Locate and identify every blood parasite.
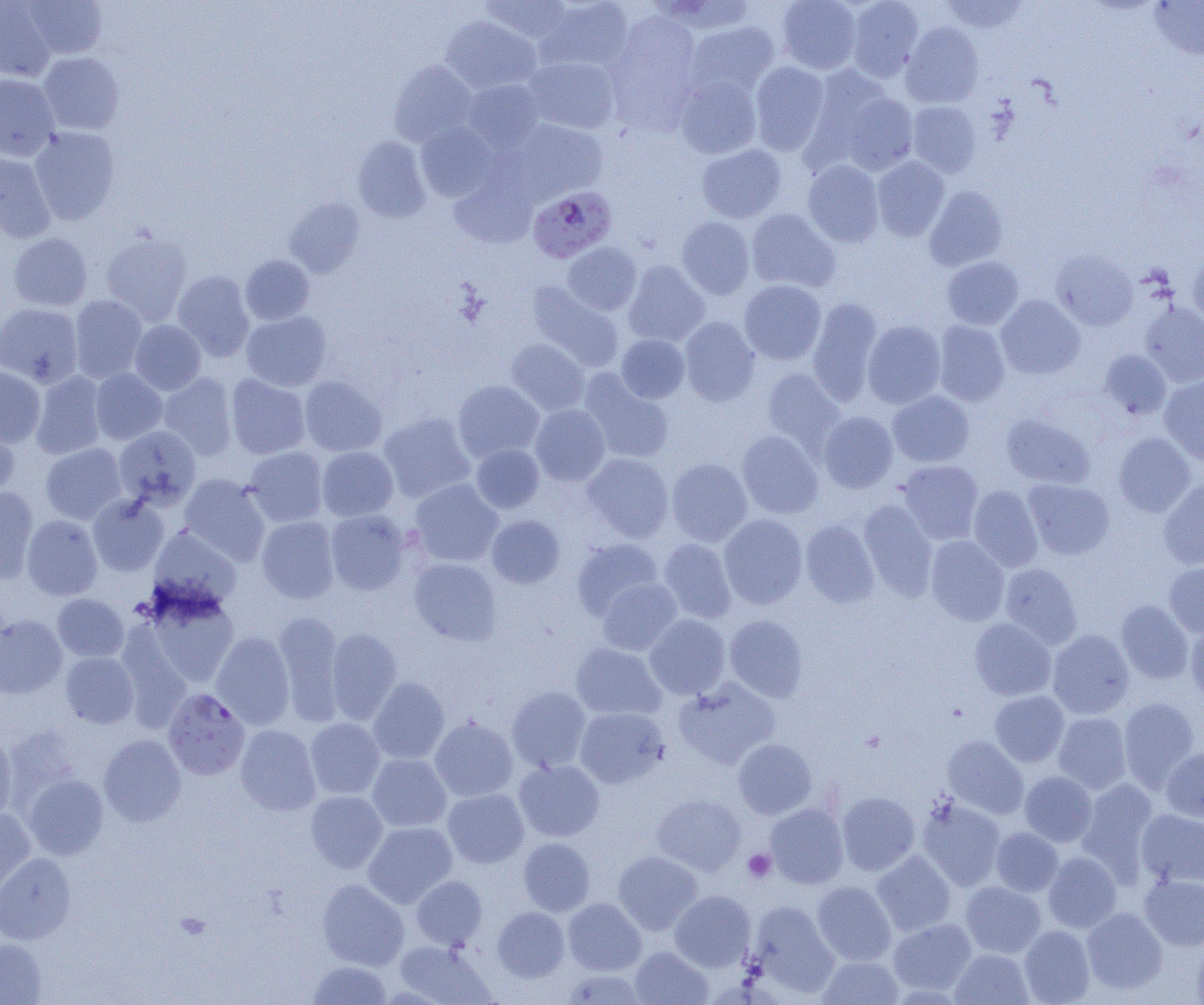

Approximate bounding boxes as (x1,y1)-(x2,y2) corner pairs in pixels.
Plasmodium falciparum-infected red blood cells: (528,186)-(616,262), (163,688)-(250,780).
No Plasmodium ovale, Plasmodium malariae, Plasmodium vivax, Babesia divergens, or Trypanosoma brucei observed.

Uninfected red blood cell locations: (22,0)-(107,59), (480,0)-(572,44), (536,0)-(634,73), (663,0)-(758,34), (776,0)-(862,73), (845,0)-(923,81), (0,1)-(57,81), (939,1)-(1029,35), (1149,1)-(1204,60), (605,13)-(703,126), (441,16)-(541,94), (686,21)-(780,97), (901,22)-(984,108), (38,52)-(124,134), (524,56)-(620,134), (389,60)-(478,146), (750,61)-(830,155), (0,73)-(60,161), (674,74)-(761,159), (461,79)-(545,153), (824,82)-(920,176), (907,101)-(982,177), (511,119)-(608,201), (415,122)-(499,202), (29,127)-(120,225), (352,136)-(431,222), (696,143)-(786,223), (0,149)-(55,243), (872,156)-(950,241), (803,160)-(884,247), (449,172)-(537,249), (924,186)-(1008,271), (284,198)-(365,278), (746,209)-(841,293), (676,216)-(755,300), (7,232)-(93,311), (100,233)-(193,325), (562,242)-(642,315), (1187,249)-(1204,329), (1051,250)-(1138,331), (240,255)-(314,325), (941,256)-(1024,330), (623,260)-(710,347), (172,270)-(254,361), (739,279)-(826,365), (526,281)-(624,372), (69,295)-(147,383), (995,295)-(1085,379), (807,297)-(884,407), (0,302)-(82,387), (1140,302)-(1204,387), (241,311)-(332,391), (679,316)-(760,406), (130,320)-(206,395), (862,320)-(946,409), (932,321)-(1010,406), (616,334)-(690,403), (505,338)-(590,416), (1098,349)-(1171,420), (0,366)-(45,447), (761,367)-(846,456), (90,368)-(167,444), (579,370)-(674,464), (31,371)-(107,459), (158,373)-(237,460), (225,374)-(311,460), (299,375)-(387,457), (1160,376)-(1204,466), (453,380)-(545,462), (887,390)-(974,467), (530,404)-(610,486), (818,411)-(898,493), (378,412)-(476,503), (1001,413)-(1095,488), (0,423)-(19,503), (113,425)-(201,510), (737,430)-(823,519), (1113,433)-(1196,517), (40,443)-(126,523), (471,444)-(544,513), (317,446)-(398,521), (243,447)-(328,527), (582,453)-(674,543), (667,458)-(752,546), (897,460)-(984,544), (179,474)-(270,566), (1158,478)-(1204,569), (409,479)-(503,567), (1023,479)-(1115,560), (968,485)-(1043,572), (0,486)-(39,582), (88,494)-(169,576), (858,500)-(938,600), (325,509)-(412,595), (487,514)-(565,589), (718,514)-(808,609), (21,515)-(102,600), (256,516)-(339,604), (800,519)-(879,608), (148,526)-(242,611), (926,535)-(1010,625), (571,538)-(664,621), (658,538)-(736,623), (409,558)-(502,645), (999,562)-(1082,649), (1164,562)-(1204,637), (596,578)-(682,656), (140,589)-(240,689), (52,593)-(128,661), (1116,600)-(1193,684), (273,612)-(345,726), (0,614)-(67,698), (644,614)-(730,699), (725,615)-(808,702), (969,617)-(1056,701), (1185,621)-(1204,707), (125,625)-(196,738), (326,627)-(402,725), (1047,629)-(1134,719), (211,631)-(295,729), (570,643)-(666,720), (60,652)-(139,728), (368,677)-(450,764), (674,678)-(780,769), (506,686)-(591,772), (989,690)-(1069,767), (1118,696)-(1201,791), (574,707)-(668,788), (1052,712)-(1131,793), (430,717)-(518,802), (305,718)-(385,799), (235,724)-(321,816), (0,733)-(17,823), (98,735)-(186,826), (942,735)-(1028,819), (733,738)-(817,819), (1161,747)-(1204,822), (367,753)-(451,832), (514,759)-(604,841), (1019,771)-(1097,846), (23,774)-(108,860), (1076,778)-(1159,880), (442,788)-(529,868), (306,791)-(388,873), (836,792)-(919,876), (653,794)-(746,875), (917,797)-(1006,890), (765,803)-(848,889), (0,808)-(36,901), (1136,809)-(1204,887), (363,821)-(457,908), (991,827)-(1063,896), (518,837)-(595,916), (872,850)-(956,937), (613,851)-(702,934), (1043,852)-(1122,933), (0,853)-(76,944), (1139,874)-(1204,951), (410,875)-(488,949), (317,878)-(409,970), (812,881)-(896,965), (960,881)-(1046,958), (670,890)-(755,972), (563,898)-(646,975), (746,900)-(839,998), (492,907)-(569,982), (1081,907)-(1168,994), (888,918)-(977,996), (1019,925)-(1095,1005), (0,937)-(46,1005), (1192,937)-(1204,1005), (392,940)-(496,1005), (629,946)-(713,1004), (950,948)-(1033,1005), (816,956)-(904,1005), (306,960)-(393,1004), (561,969)-(646,1005). Platelet locations: (743,849)-(776,882). Slide-level diagnosis: Plasmodium falciparum. Light microscopy. Thin blood film. Image is 1204×1005 pixels. Single field of view. Captured at 1000x magnification.